State which parasite is depicted.
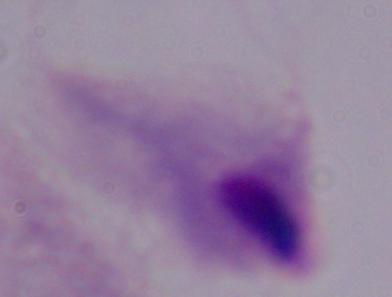

A trichomonad.

Summary:
  - Magnification: 1000x
  - Modality: micrograph